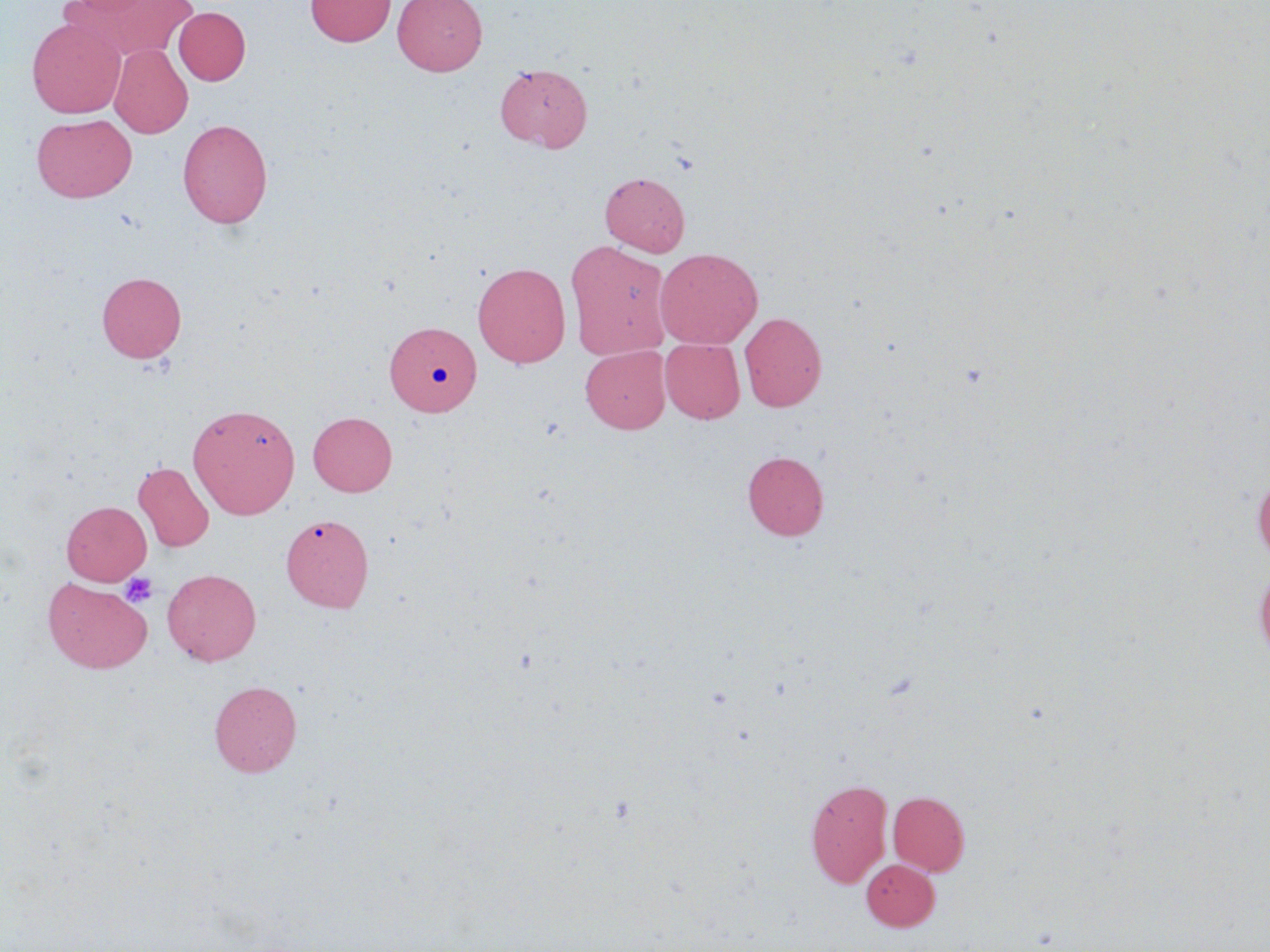
Approximate bounding boxes as [x1, y1, x2, y2] in pixels. Platelet locations: [120, 573, 157, 608]. Uninfected red blood cell locations: [66, 0, 159, 17], [69, 0, 199, 63], [305, 0, 395, 47], [393, 0, 487, 76], [173, 7, 250, 85], [27, 17, 125, 118], [109, 44, 192, 138], [495, 62, 592, 152], [32, 114, 137, 202], [177, 118, 273, 228], [600, 171, 690, 256], [565, 241, 672, 359], [655, 248, 763, 349], [472, 262, 571, 368], [96, 272, 186, 363], [739, 311, 827, 412], [385, 324, 481, 420], [660, 338, 745, 423], [581, 346, 670, 433], [187, 403, 300, 519], [308, 411, 397, 496], [742, 450, 829, 541], [133, 462, 214, 552], [1252, 473, 1270, 564], [62, 501, 151, 585], [281, 513, 373, 612], [1255, 564, 1270, 666], [162, 568, 261, 666], [43, 577, 153, 674], [209, 680, 302, 777], [806, 778, 892, 888], [888, 791, 970, 875], [861, 859, 939, 930]. Slide-level diagnosis: negative for blood parasites. Thin blood smear. May-Grünwald-Giemsa-stained preparation. Single field of view. Optical microscopy. Captured at 1000x magnification. Image is 1270×952 pixels.